Report the malaria status of this cell.
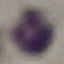

It is uninfected.

Giemsa stain. Thin blood smear. Automatically extracted cell patch, resized to 64 × 64 pixels. Photographed with a smartphone camera at the microscope eyepiece.